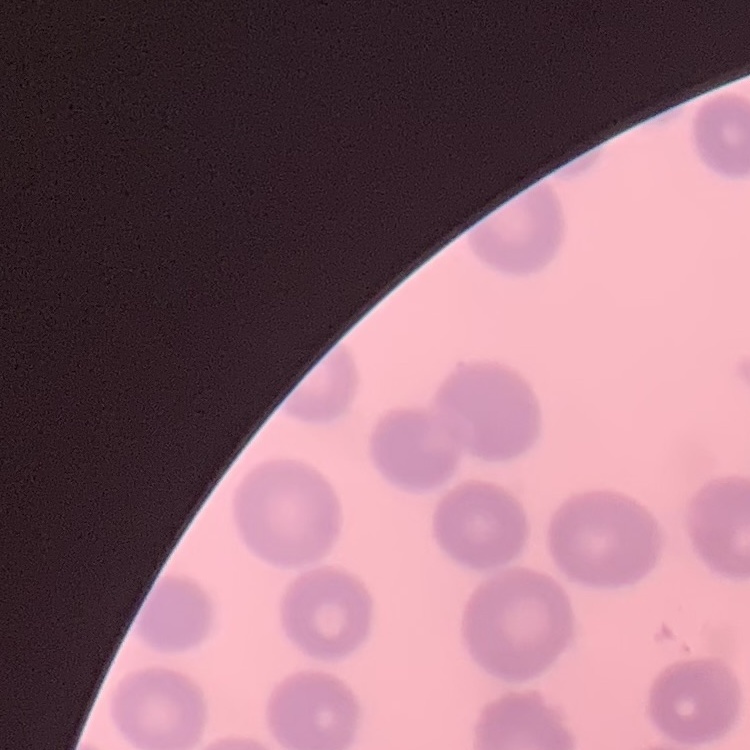

Summary:
  - Erythrocyte morphology: no rouleaux formation
  - Preparation: thin peripheral smear
  - Image type: one tile cut from a larger photomicrograph
  - Stain: Field's or Giemsa